Locate every Plasmodium parasite.
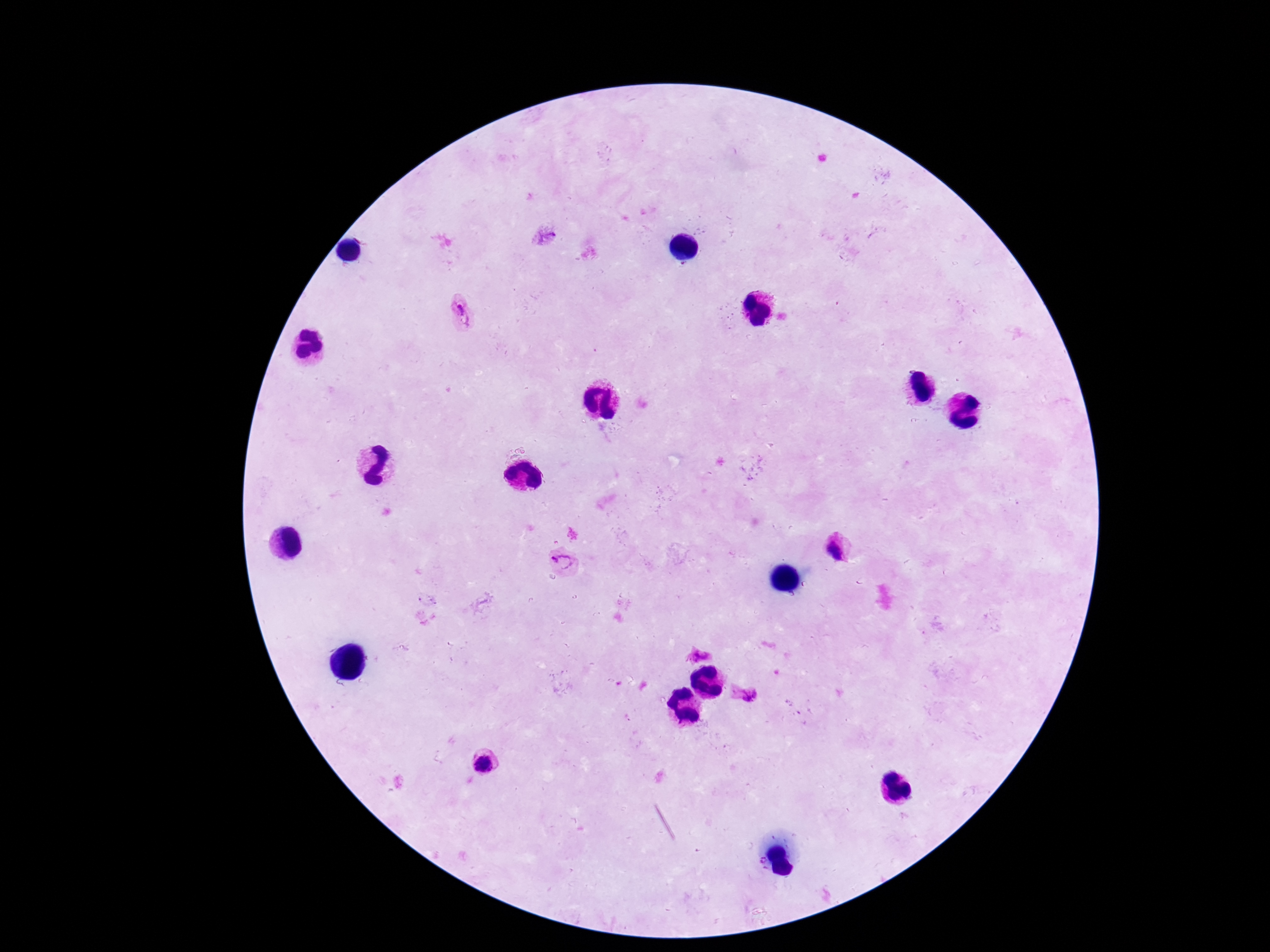

Approximate object centers, in pixels from the top-left corner.
Plasmodium parasites: (x=547, y=236), (x=464, y=313), (x=840, y=553), (x=566, y=562), (x=703, y=655), (x=751, y=697), (x=483, y=764).

Patient malaria status: infected. One field from this slide. Giemsa-stained preparation. 100x magnification. Thick blood film. Image is 1270×952 pixels. Photographed through the microscope eyepiece with a smartphone camera.